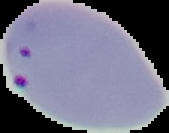

Summary:
  - Image size: 169×133 pixels
  - Image type: segmented cell region on a black background
  - Preparation: thin blood film
  - Result: Plasmodium parasites detected